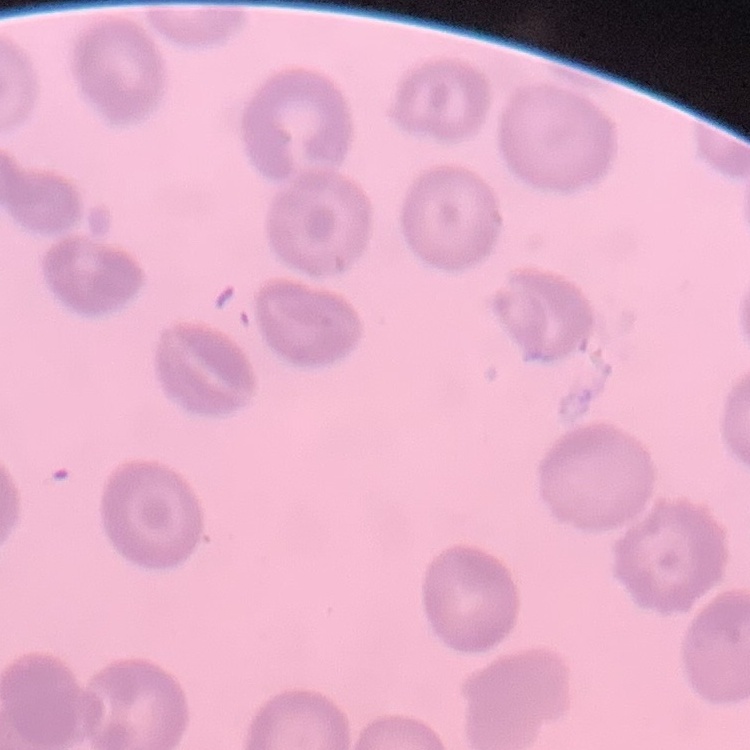

The red blood cells show no rouleaux formation. Thin blood film. One tile cut from a larger photomicrograph. Field's or Giemsa stain.